Classify this cell by malaria status.
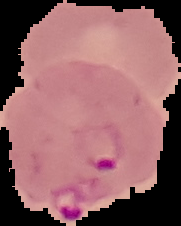

Parasitized.

Summary:
  - Preparation: thin blood film
  - Image type: segmented cell region on a black background
  - Image size: 181×226 pixels